Report the malaria status of this cell.
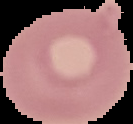

Uninfected.

image size = 133×124 pixels
image type = segmented cell region on a black background
preparation = thin blood film